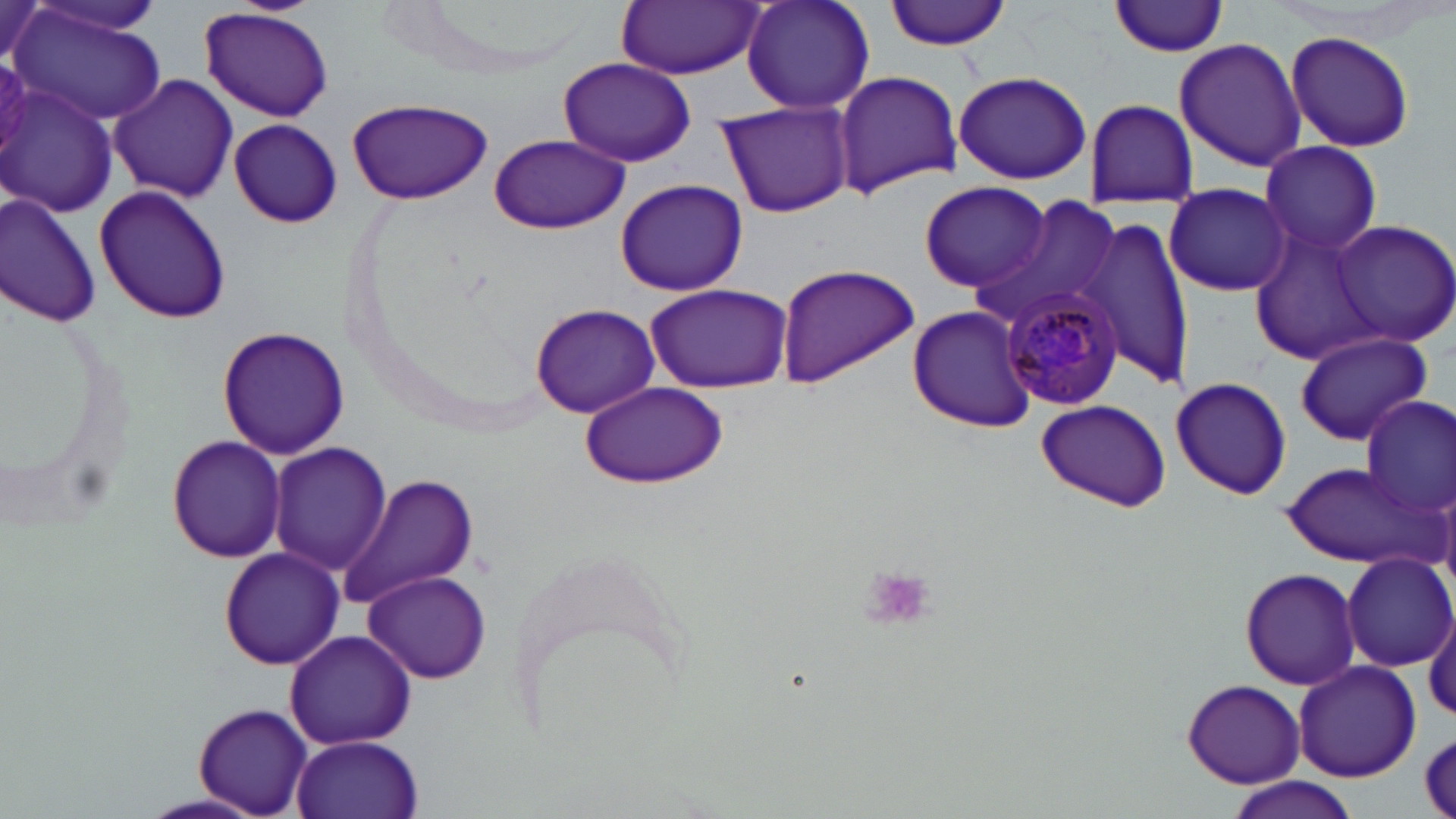

slide-level diagnosis = Plasmodium malariae
stain = May-Grünwald-Giemsa
Plasmodium malariae-infected red blood cell locations = approximate bounding boxes as named x1/y1/x2/y2 corners in pixels: (x1=1000, y1=287, x2=1124, y2=411)
preparation = thin blood smear
field of view = one of a larger specimen
image size = 1456×819 pixels
platelet locations = approximate bounding boxes as named x1/y1/x2/y2 corners in pixels: (x1=858, y1=569, x2=937, y2=633)
uninfected red blood cell locations = approximate bounding boxes as named x1/y1/x2/y2 corners in pixels: (x1=23, y1=0, x2=170, y2=41), (x1=740, y1=0, x2=876, y2=117), (x1=883, y1=0, x2=1019, y2=51), (x1=616, y1=1, x2=764, y2=79), (x1=1109, y1=1, x2=1234, y2=57), (x1=2, y1=3, x2=51, y2=74), (x1=10, y1=6, x2=169, y2=126), (x1=197, y1=8, x2=334, y2=122), (x1=1284, y1=31, x2=1416, y2=153), (x1=1174, y1=37, x2=1307, y2=174), (x1=556, y1=56, x2=695, y2=166), (x1=833, y1=69, x2=962, y2=197), (x1=952, y1=69, x2=1094, y2=186), (x1=109, y1=71, x2=235, y2=203), (x1=5, y1=82, x2=119, y2=218), (x1=348, y1=97, x2=493, y2=204), (x1=1083, y1=100, x2=1199, y2=207), (x1=715, y1=102, x2=853, y2=217), (x1=228, y1=118, x2=342, y2=229), (x1=489, y1=133, x2=627, y2=235), (x1=1260, y1=140, x2=1385, y2=257), (x1=614, y1=179, x2=748, y2=297), (x1=917, y1=180, x2=1052, y2=294), (x1=94, y1=183, x2=232, y2=324), (x1=1162, y1=183, x2=1293, y2=297), (x1=0, y1=193, x2=101, y2=327), (x1=974, y1=197, x2=1119, y2=331), (x1=1082, y1=214, x2=1194, y2=389), (x1=1328, y1=221, x2=1456, y2=350), (x1=1248, y1=223, x2=1388, y2=366), (x1=774, y1=261, x2=918, y2=385), (x1=643, y1=282, x2=793, y2=392), (x1=529, y1=302, x2=661, y2=417), (x1=907, y1=304, x2=1038, y2=431), (x1=215, y1=324, x2=350, y2=462), (x1=1295, y1=329, x2=1432, y2=447), (x1=1170, y1=376, x2=1292, y2=501), (x1=577, y1=381, x2=728, y2=489), (x1=1359, y1=395, x2=1455, y2=524), (x1=1033, y1=399, x2=1172, y2=513), (x1=166, y1=433, x2=289, y2=563), (x1=268, y1=442, x2=392, y2=575), (x1=1279, y1=459, x2=1436, y2=570), (x1=338, y1=473, x2=480, y2=607), (x1=217, y1=545, x2=343, y2=670), (x1=1341, y1=551, x2=1455, y2=672), (x1=1240, y1=568, x2=1360, y2=691), (x1=362, y1=570, x2=491, y2=683), (x1=1425, y1=609, x2=1456, y2=729), (x1=283, y1=629, x2=417, y2=752), (x1=1292, y1=661, x2=1423, y2=785), (x1=1180, y1=678, x2=1305, y2=787), (x1=192, y1=702, x2=315, y2=818), (x1=1417, y1=729, x2=1456, y2=813), (x1=292, y1=734, x2=423, y2=819), (x1=1223, y1=775, x2=1363, y2=819)
modality = optical microscopy
magnification = 1000x